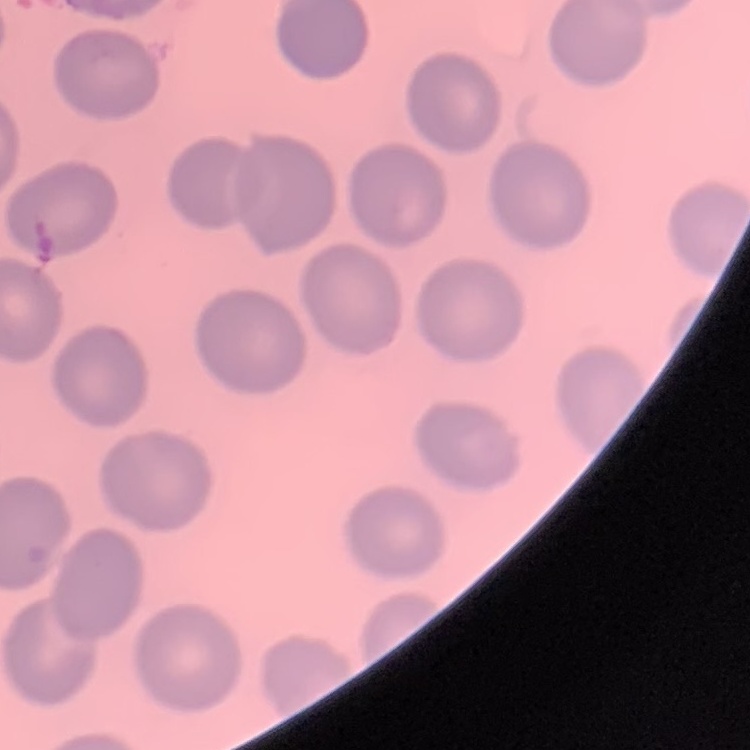

{
  "red_blood_cell_morphology": "no rouleaux formation",
  "image_type": "one tile cut from a larger photomicrograph",
  "preparation": "thin peripheral smear",
  "stain": "Field's or Giemsa"
}